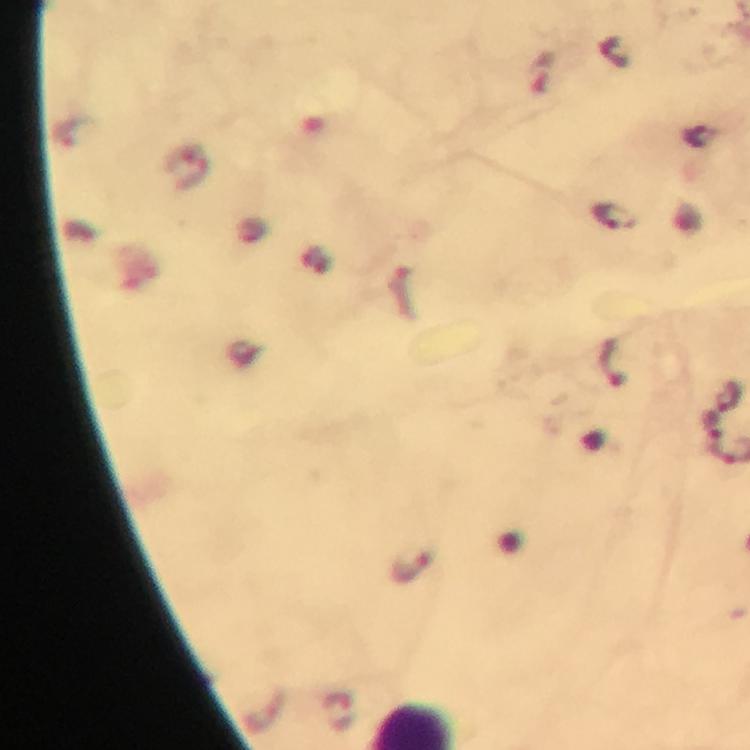

Approximate centers as {x, y} in pixels.
Summary:
  - Malaria parasite locations: {613, 216}, {727, 394}, {712, 423}, {410, 567}, {337, 712}
  - Immersion oil: used
  - Cropped from: a single field of view
  - Magnification: 100x
  - Preparation: thick blood film
  - Context: from a diagnostic examination for malaria
  - Stain: Giemsa
  - Capture: smartphone photograph through a microscope
  - Image size: 750×750 pixels